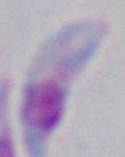

1000x magnification. Micrograph. Toxoplasma gondii is shown.